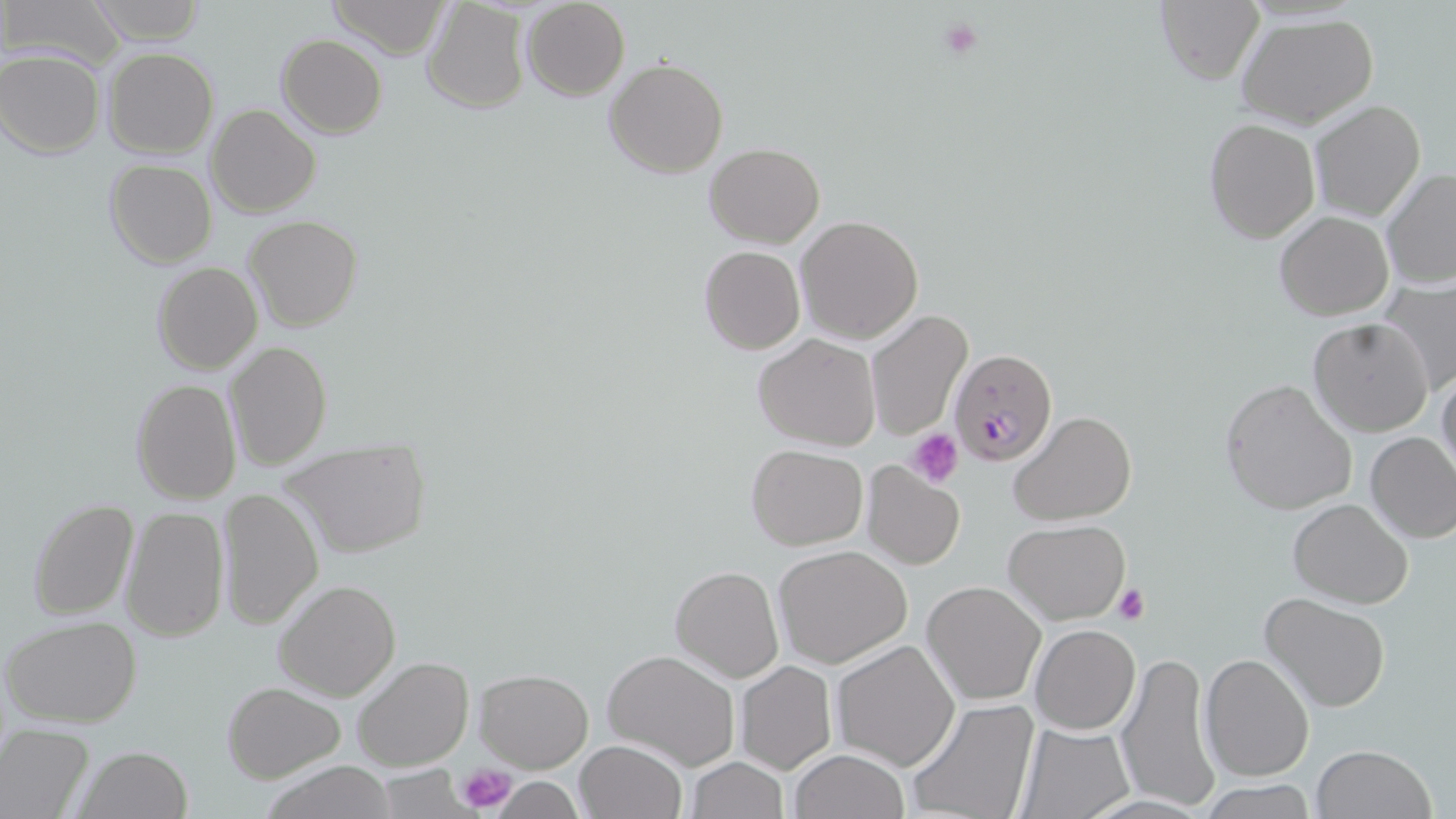
slide-level diagnosis = Plasmodium falciparum
preparation = thin blood smear
magnification = 1000x
image size = 1456×819 pixels
field of view = single
Plasmodium falciparum-infected red blood cell locations = approximate bounding boxes as (x1, y1, x2, y2) in pixels: (948, 348, 1058, 466)
modality = light microscopy
platelet locations = approximate bounding boxes as (x1, y1, x2, y2) in pixels: (937, 18, 982, 62), (909, 430, 964, 487), (1113, 585, 1149, 625), (456, 762, 517, 813)
stain = May-Grünwald-Giemsa
uninfected red blood cell locations = approximate bounding boxes as (x1, y1, x2, y2) in pixels: (8, 0, 122, 66), (85, 0, 206, 43), (325, 0, 454, 57), (521, 0, 630, 101), (1155, 0, 1264, 86), (422, 2, 531, 114), (1236, 14, 1380, 131), (276, 35, 386, 138), (103, 46, 218, 159), (1, 50, 105, 158), (604, 59, 729, 179), (1309, 100, 1427, 221), (206, 103, 320, 219), (1203, 117, 1321, 243), (704, 143, 825, 247), (104, 159, 216, 268), (1383, 168, 1454, 292), (1274, 210, 1394, 319), (796, 214, 924, 344), (244, 216, 363, 331), (698, 245, 805, 354), (152, 261, 262, 375), (1380, 282, 1456, 393), (865, 310, 974, 442), (1307, 317, 1435, 437), (753, 334, 881, 452), (226, 341, 333, 471), (1436, 368, 1456, 484), (131, 378, 241, 506), (1219, 379, 1357, 516), (1011, 410, 1135, 525), (1365, 431, 1456, 544), (279, 437, 430, 559), (746, 444, 868, 549), (861, 462, 966, 569), (218, 489, 323, 628), (1287, 498, 1414, 607), (27, 499, 138, 621), (119, 506, 229, 642), (1003, 518, 1132, 623), (772, 545, 912, 668), (669, 565, 783, 684), (272, 580, 401, 701), (922, 580, 1047, 706), (1262, 595, 1389, 714), (3, 616, 143, 728), (1030, 623, 1141, 733), (831, 639, 961, 772), (601, 648, 740, 771), (1116, 648, 1224, 811), (1199, 653, 1315, 783), (353, 656, 475, 771), (734, 660, 836, 775), (476, 669, 593, 771), (222, 681, 346, 783), (905, 698, 1041, 819), (1016, 720, 1137, 819), (0, 725, 95, 819), (573, 740, 687, 819), (1310, 743, 1436, 819), (76, 744, 193, 818), (788, 749, 909, 819), (686, 758, 788, 818), (259, 762, 400, 819), (493, 777, 584, 818), (1200, 781, 1321, 818)